Classify this cell by malaria status.
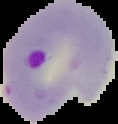
It is parasitized.

{
  "preparation": "thin blood smear",
  "image_size": "118×124 pixels",
  "image_type": "segmented cell region on a black background"
}